Comment on the morphology of the erythrocytes.
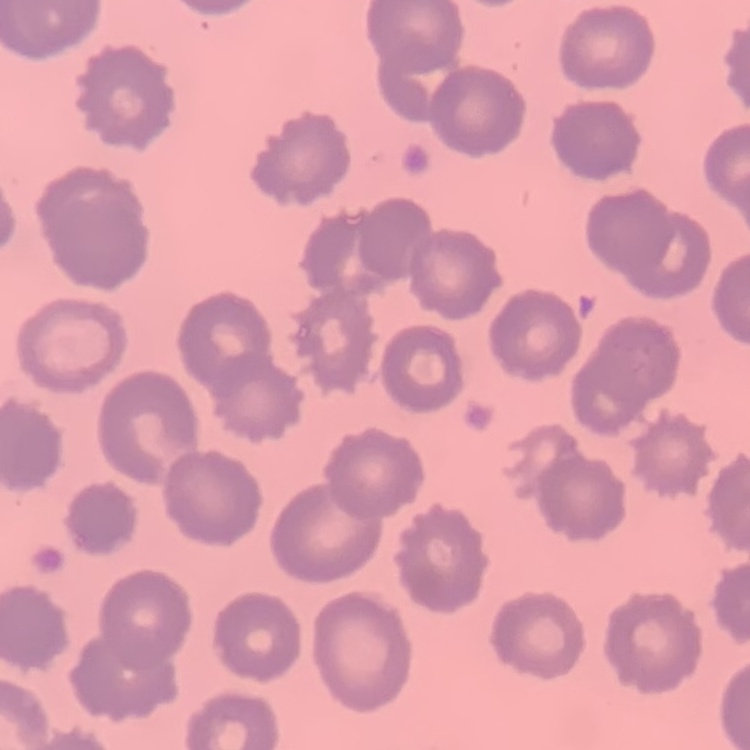
No rouleaux formation.

Square crop of a larger photomicrograph. Field's or Giemsa stain. Thin blood film.